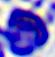
{
  "modality": "micrograph",
  "magnification": "400x",
  "identification": "white blood cell"
}